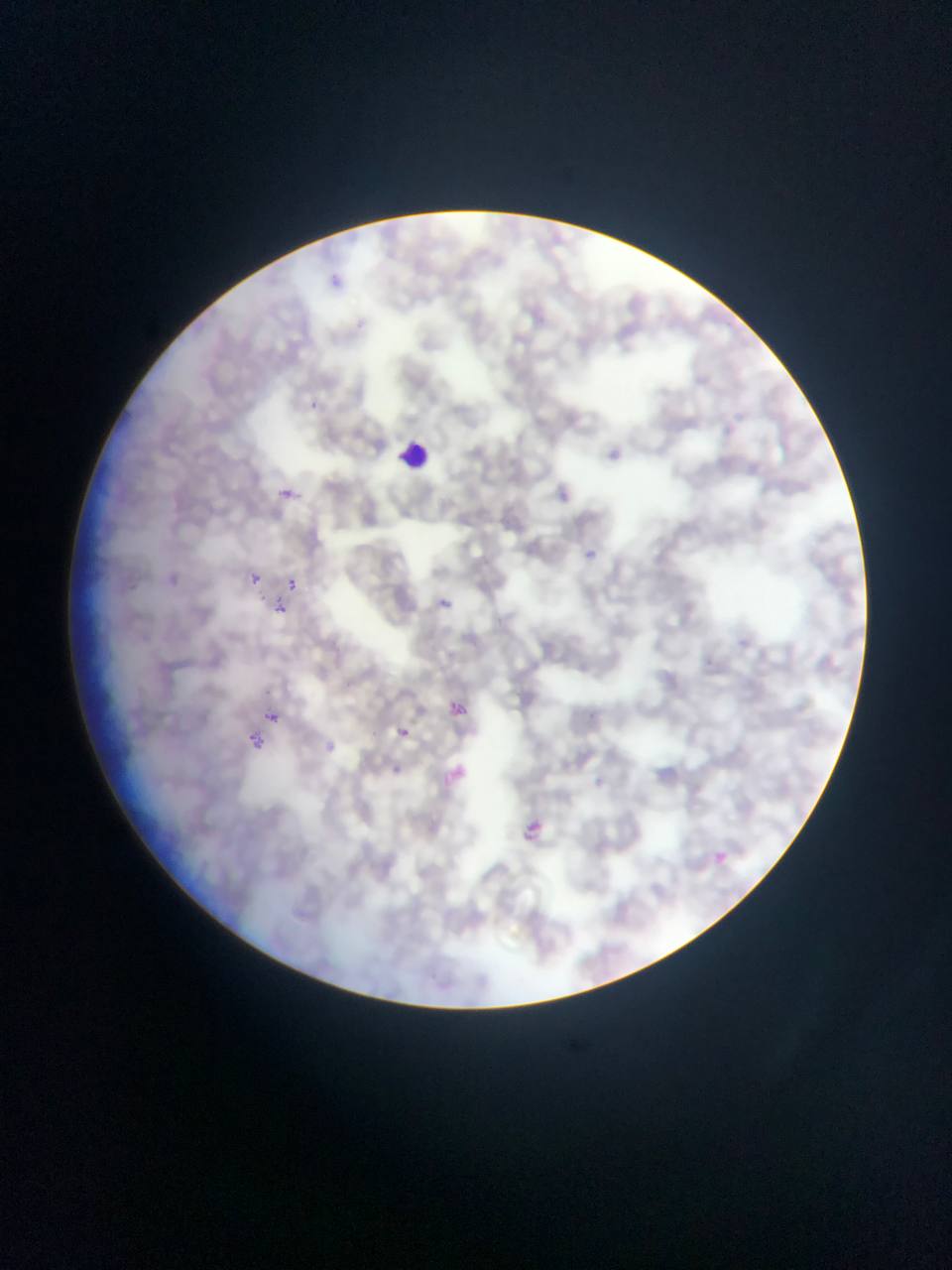
Approximate bounding boxes as left top right bottom in pixels.
Summary:
  - Leukocyte locations: 394 436 438 477
  - Malaria parasite locations: 300 394 324 417; 584 548 599 562; 161 572 181 590; 249 574 260 585; 286 579 297 590; 283 580 299 595; 441 595 453 611; 273 604 287 616; 270 713 279 729; 395 725 412 741; 245 733 264 751; 318 737 341 759; 438 761 471 794; 386 762 405 778; 516 816 551 849; 711 849 729 866
  - Capture: mobile-phone photograph through a microscope
  - Preparation: thin blood smear
  - Country: Ghana
  - Field of view: single
  - Image size: 952×1270 pixels